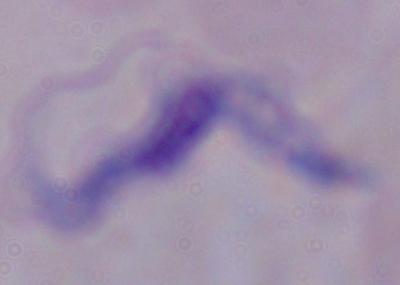
modality: photomicrograph
identification: trypanosome
magnification: 1000x